Report the malaria status of this cell.
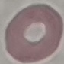
It is uninfected.

{
  "stain": "Giemsa",
  "capture": "smartphone camera at the microscope eyepiece",
  "image_type": "automatically extracted cell patch, resized to 64 × 64 pixels",
  "preparation": "thin smear"
}